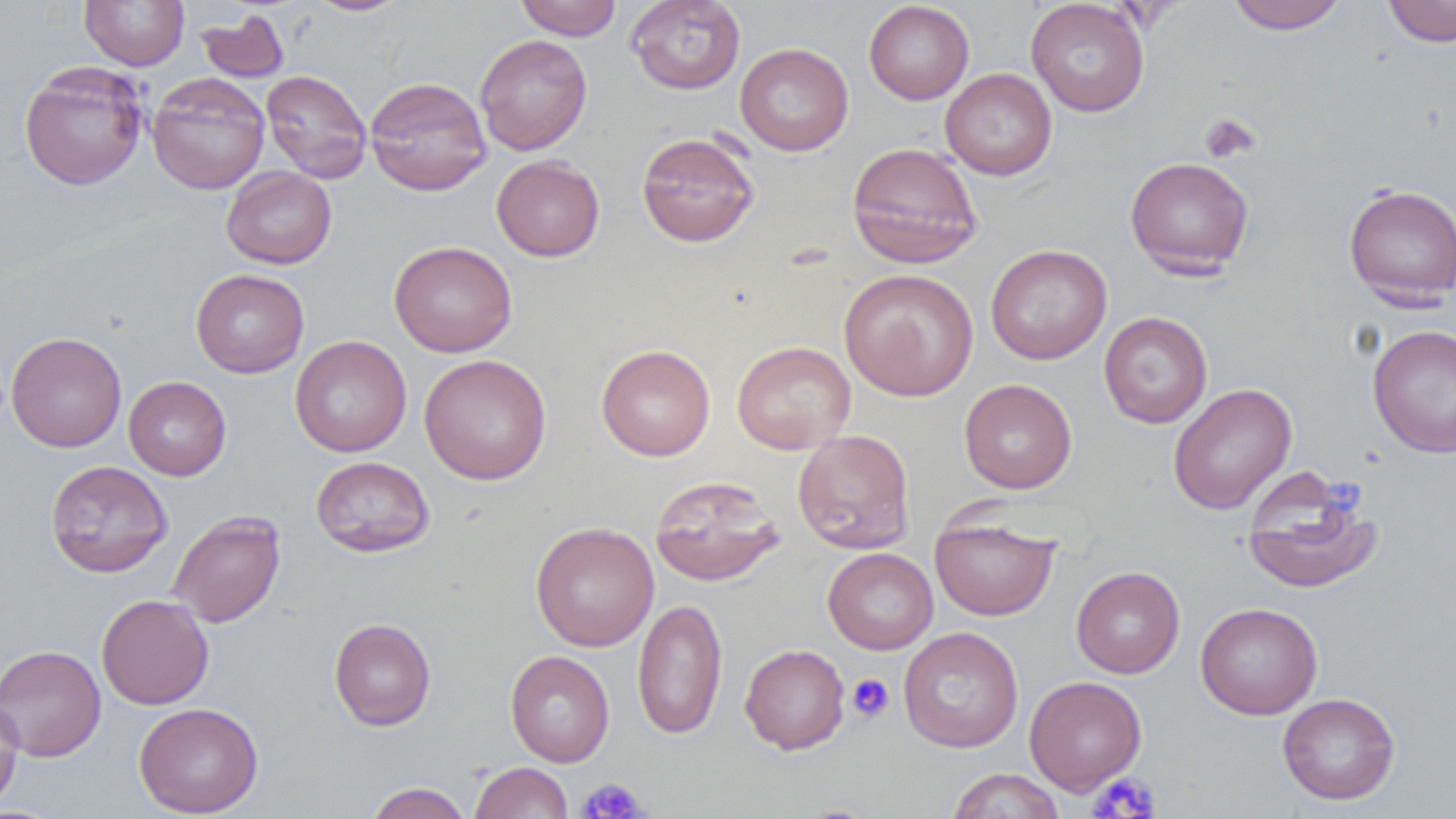
Summary:
  - Coordinate format: approximate bounding boxes as [x1, y1, x2, y2] in pixels
  - Platelet locations: [1199, 113, 1260, 164], [847, 674, 893, 723], [1088, 773, 1161, 818], [578, 778, 650, 819]
  - Uninfected red blood cell locations: [79, 0, 189, 70], [305, 0, 414, 16], [515, 0, 622, 40], [625, 0, 746, 95], [1224, 0, 1350, 34], [1382, 0, 1456, 47], [863, 1, 974, 105], [1025, 1, 1150, 117], [195, 9, 290, 83], [475, 34, 592, 156], [735, 42, 854, 156], [19, 61, 149, 191], [940, 67, 1057, 180], [260, 69, 372, 183], [146, 73, 270, 195], [365, 76, 491, 195], [636, 130, 760, 248], [846, 142, 983, 269], [491, 155, 605, 262], [1125, 156, 1254, 278], [221, 166, 337, 269], [1342, 183, 1456, 307], [389, 240, 517, 357], [985, 244, 1112, 365], [838, 268, 978, 400], [191, 269, 309, 378], [1098, 311, 1213, 428], [1367, 324, 1456, 458], [6, 331, 126, 452], [290, 335, 412, 457], [732, 340, 856, 454], [596, 344, 715, 461], [419, 353, 551, 485], [124, 376, 231, 480], [959, 378, 1077, 494], [1168, 383, 1297, 514], [792, 429, 915, 554], [310, 455, 435, 557], [45, 460, 173, 578], [1240, 465, 1383, 595], [650, 475, 785, 587], [167, 510, 286, 628], [930, 515, 1060, 621], [530, 521, 659, 651], [823, 547, 939, 654], [1071, 565, 1185, 678], [96, 594, 214, 710], [632, 598, 727, 740], [1195, 602, 1323, 719], [329, 618, 436, 731], [898, 626, 1024, 753], [0, 644, 106, 762], [739, 644, 850, 754], [505, 650, 614, 767], [1024, 675, 1147, 795], [1277, 692, 1400, 805], [0, 698, 25, 816], [134, 702, 264, 817], [469, 761, 573, 819], [947, 768, 1065, 819], [364, 782, 472, 819]
  - Slide-level diagnosis: no evidence of blood parasites
  - Modality: light microscopy
  - Preparation: thin blood smear
  - Image size: 1456×819 pixels
  - Magnification: 1000x
  - Field of view: single